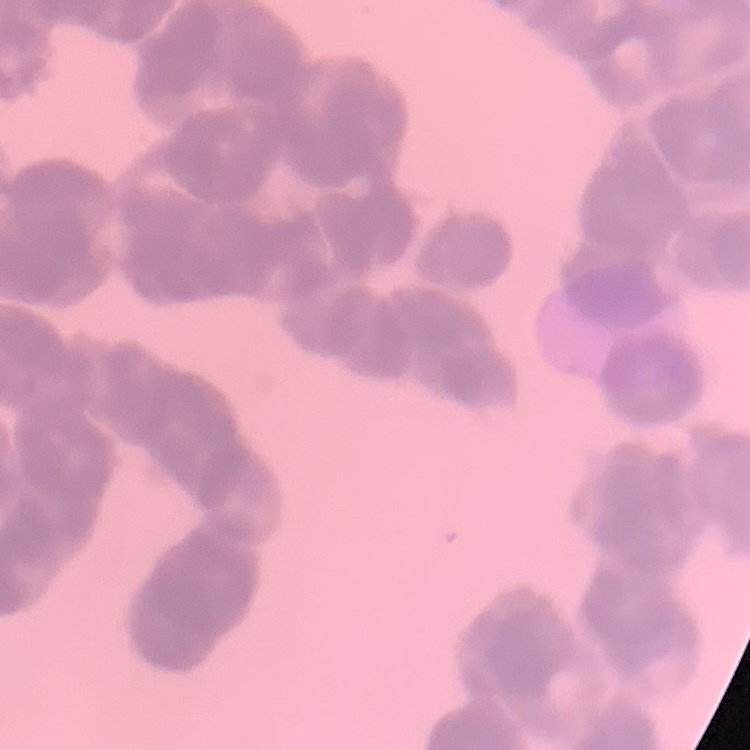
Summary:
  - Red blood cell morphology: rouleaux formation
  - Stain: Field's or Giemsa
  - Image type: square crop of a larger photomicrograph
  - Preparation: thin blood film